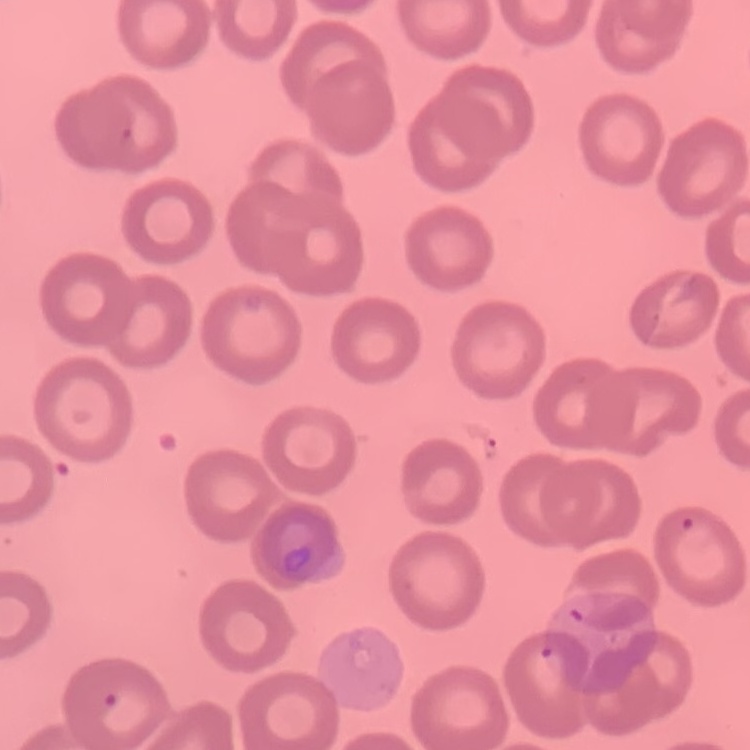
The erythrocytes show no rouleaux formation. Square crop of a larger photomicrograph. Thin peripheral smear. Field's or Giemsa stain.